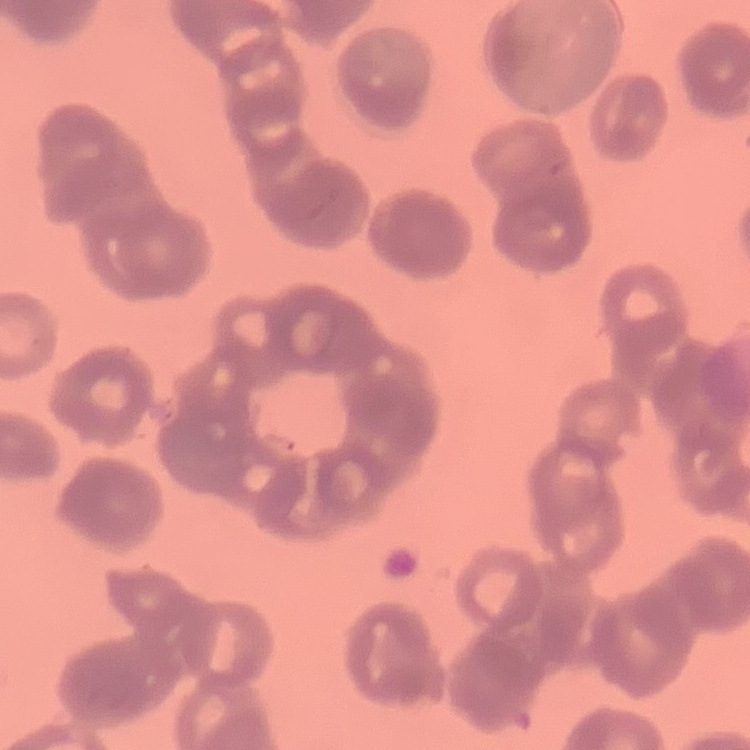
Summary:
  - Erythrocyte morphology: rouleaux formation
  - Preparation: thin peripheral smear
  - Stain: Field's or Giemsa
  - Image type: one tile cut from a larger photomicrograph